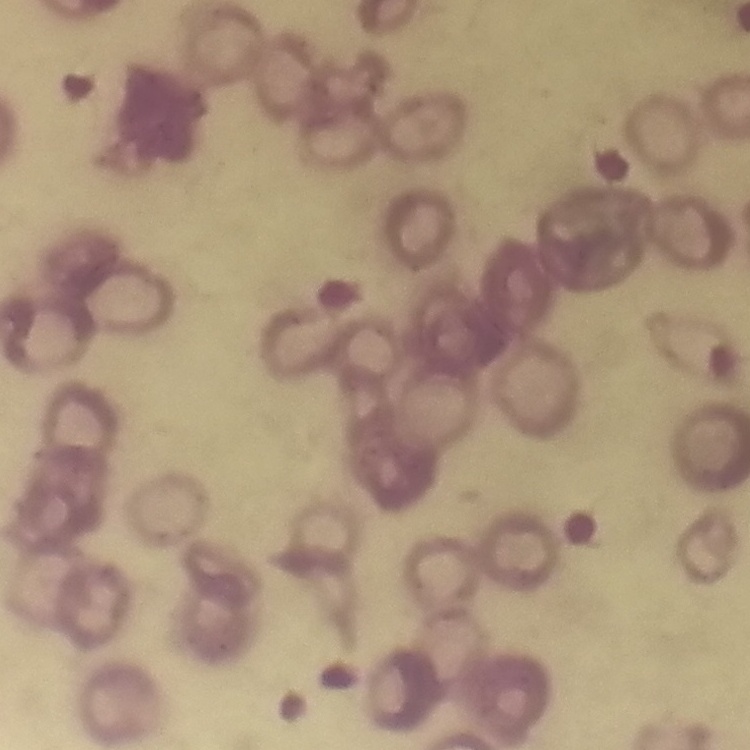
The red blood cells exhibit rouleaux formation. Stained with either Field's or Giemsa. Square crop of a larger photomicrograph. Thin blood smear.